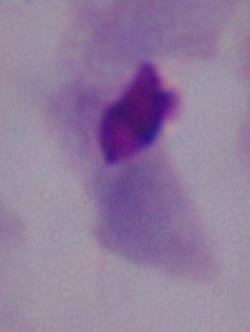
identification = trichomonad
magnification = 1000x
modality = photomicrograph